Outline each blood parasite and name the species.
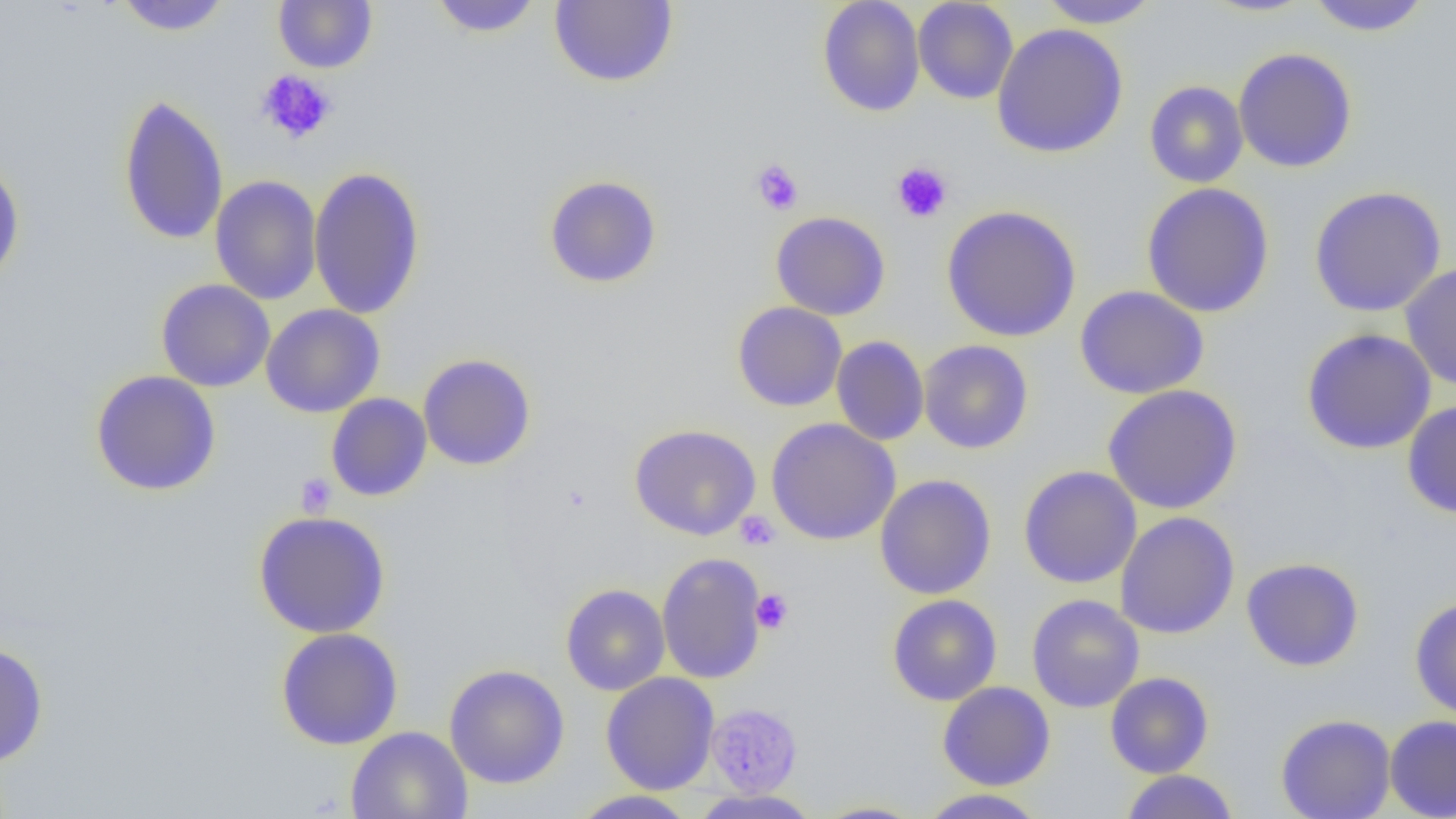
No blood parasites observed.

Summary:
  - Coordinate format: approximate bounding boxes as [x1, y1, x2, y2] in pixels
  - Uninfected red blood cell locations: [113, 0, 231, 36], [273, 0, 378, 73], [428, 0, 543, 38], [549, 0, 679, 88], [817, 0, 925, 117], [912, 0, 1018, 104], [1036, 0, 1163, 29], [1199, 0, 1318, 17], [1305, 0, 1432, 36], [991, 23, 1129, 159], [1233, 47, 1358, 174], [1144, 80, 1249, 188], [118, 93, 229, 246], [0, 156, 25, 288], [308, 166, 425, 321], [210, 175, 323, 305], [543, 175, 662, 289], [1141, 182, 1275, 318], [1309, 186, 1447, 317], [941, 205, 1082, 342], [770, 211, 891, 320], [1400, 262, 1456, 391], [156, 279, 275, 392], [1075, 285, 1209, 400], [732, 302, 847, 412], [261, 304, 385, 418], [1301, 327, 1437, 455], [831, 336, 930, 446], [918, 339, 1034, 454], [417, 354, 536, 471], [90, 370, 222, 496], [1102, 384, 1242, 514], [326, 393, 432, 502], [1402, 399, 1456, 519], [766, 417, 901, 545], [629, 424, 761, 540], [1018, 466, 1142, 588], [874, 473, 997, 600], [252, 510, 391, 638], [1115, 511, 1240, 639], [656, 552, 769, 685], [1241, 557, 1365, 671], [560, 583, 670, 696], [887, 594, 1002, 706], [1026, 594, 1144, 713], [1409, 596, 1456, 722], [275, 627, 404, 750], [0, 641, 49, 767], [444, 663, 570, 789], [601, 672, 719, 795], [1105, 672, 1214, 778], [937, 681, 1056, 790], [1276, 713, 1396, 819], [1385, 715, 1456, 818], [345, 726, 472, 819], [1119, 770, 1239, 818], [917, 788, 1049, 818], [694, 789, 818, 818], [569, 790, 698, 819], [811, 800, 927, 818]
  - Platelet locations: [255, 69, 337, 145], [750, 159, 804, 216], [891, 161, 953, 223], [296, 473, 337, 518], [735, 511, 780, 551], [751, 589, 793, 634], [711, 707, 802, 796]
  - Slide-level diagnosis: negative for blood parasites
  - Modality: optical microscopy
  - Magnification: 1000x
  - Preparation: thin blood film
  - Image size: 1456×819 pixels
  - Field of view: one of a larger specimen